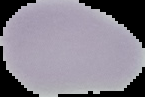
From a thin blood smear. Segmented cell region on a black background. Result: no malaria parasites seen. Image is 145×97 pixels.